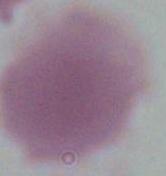
A red blood cell is seen. Photomicrograph. 1000x magnification.